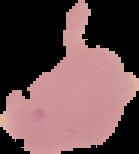
Image is 139×154 pixels. The area outside the segmented cell region is set to black. From a thin blood film. Malaria status: uninfected.